Classify this cell by malaria status.
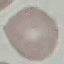
It is uninfected.

capture: smartphone through the microscope eyepiece
preparation: thin smear
image_type: automatically extracted cell patch, resized to 64 × 64 pixels
stain: Giemsa